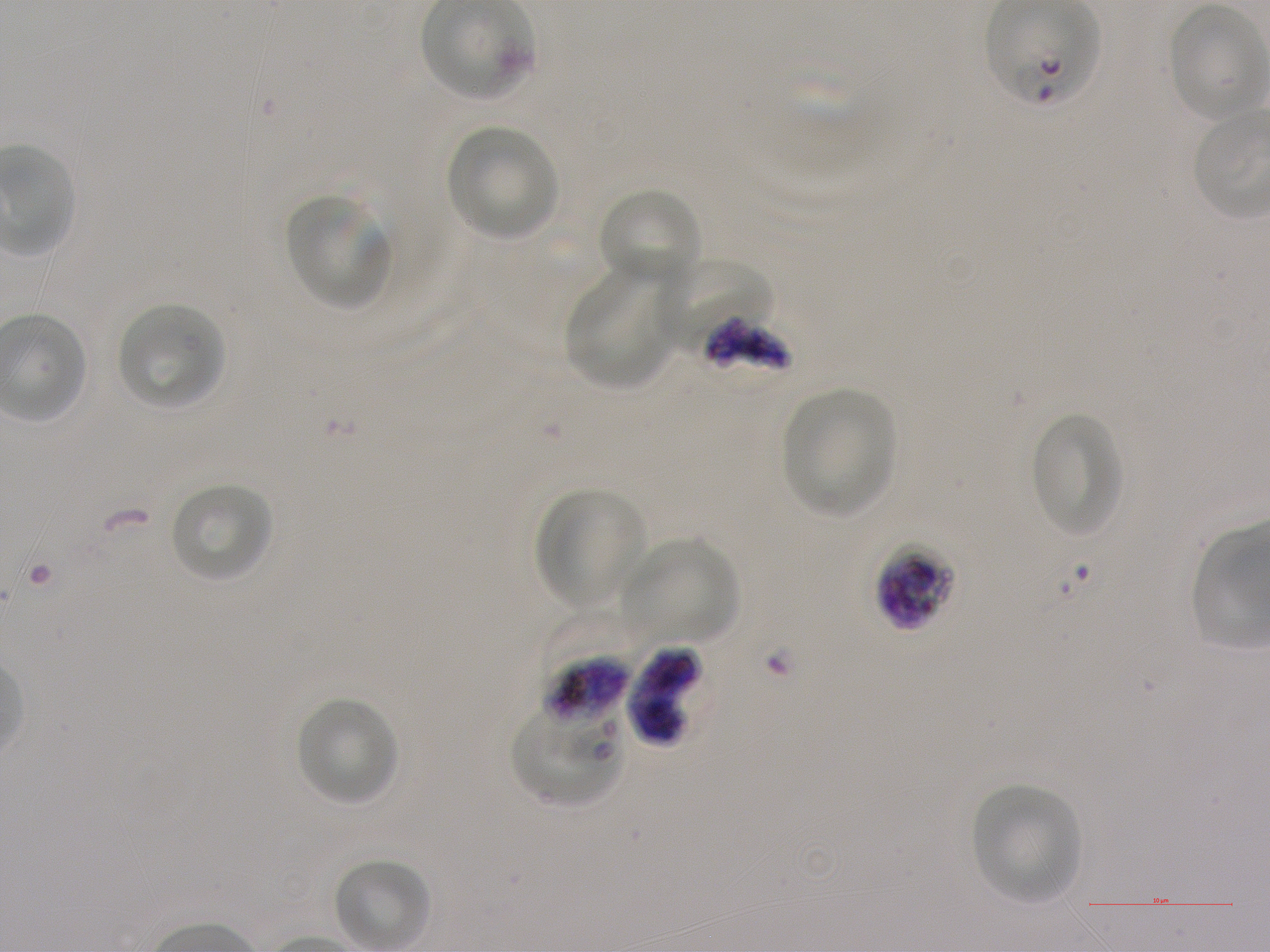 Approximate bounding boxes as (x1, y1, x2, y2) in pixels. Not every red blood cell is marked. A life-cycle stage — or a range of stages, where the recorded stages span more than one — follows each staged infected red blood cell. Locations of uninfected red blood cells: (422, 0, 533, 101), (1169, 6, 1268, 121), (448, 126, 558, 239), (597, 188, 700, 288), (285, 196, 389, 310), (566, 271, 674, 390), (117, 303, 227, 410), (784, 388, 893, 517), (1030, 414, 1124, 539), (170, 483, 273, 583), (536, 488, 647, 610), (621, 538, 739, 643), (295, 697, 400, 806), (971, 785, 1081, 903), (332, 858, 430, 951). Locations of infected red blood cells: (988, 0, 1099, 107); (875, 542, 957, 631) schizont; (627, 647, 710, 747). Locations of red blood cells of indeterminate infection status: (657, 257, 773, 349), (698, 316, 793, 371), (536, 611, 645, 722), (510, 706, 622, 805). Image is 1270×952 pixels. Single field of view. Giemsa-stained preparation. Blood group of the donor: A+. Thin blood smear. 100x objective under oil immersion, numerical aperture 1.25. P. falciparum strain NF54 in static in-vitro culture.